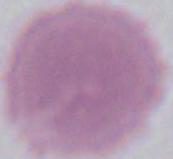

identification = erythrocyte
magnification = 1000x
modality = photomicrograph